Assess this cell for malaria.
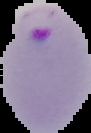
It is parasitized.

Summary:
  - Image size: 91×133 pixels
  - Preparation: thin blood smear
  - Image type: segmented cell region on a black background